Report the malaria status of this cell.
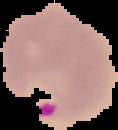

It is parasitized.

image type = segmented cell region with the area outside set to black
image size = 118×130 pixels
preparation = thin blood film